Locate every Plasmodium parasite.
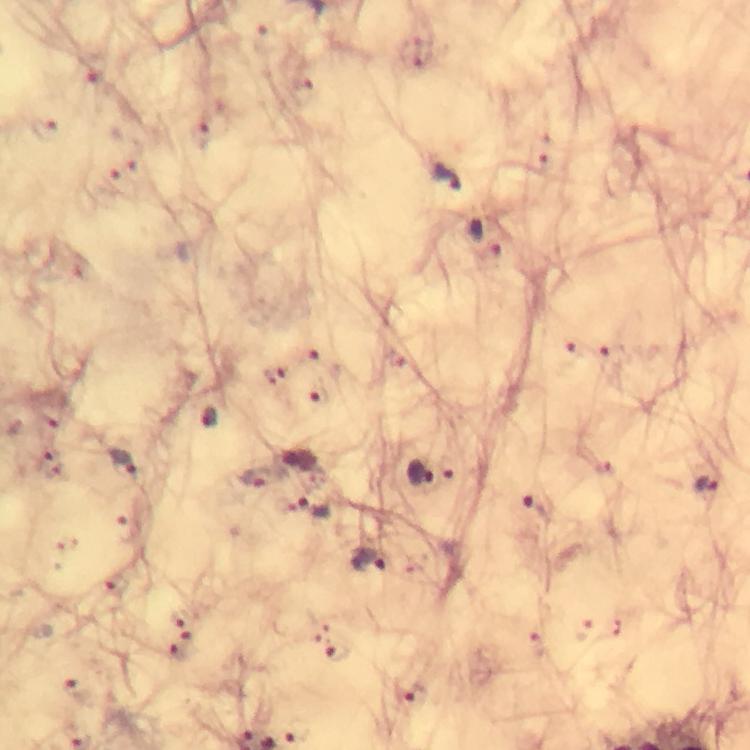

Approximate centers as {x, y} in pixels.
Plasmodium parasites: {93, 65}, {306, 91}, {45, 131}, {200, 134}, {134, 160}, {446, 176}, {112, 179}, {485, 239}, {569, 353}, {309, 355}, {612, 356}, {276, 375}, {321, 394}, {208, 417}, {122, 461}, {48, 465}, {448, 467}, {602, 467}, {417, 474}, {256, 475}, {705, 483}, {307, 509}, {535, 509}, {130, 526}, {367, 561}, {117, 584}, {180, 619}, {190, 637}, {180, 652}, {336, 652}, {78, 690}, {415, 695}.

stain = Giemsa
cropped from = one field of view
preparation = thick blood smear
image size = 750×750 pixels
immersion oil = used
context = from a malaria diagnostic workup
magnification = 100x
capture = smartphone mounted on the microscope